Report the malaria status of this cell.
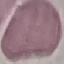
It is uninfected.

preparation = thin smear
capture = smartphone camera at the microscope eyepiece
stain = Giemsa
image type = automatically extracted cell patch, resized to 64 × 64 pixels